Assess the morphology of the red blood cells.
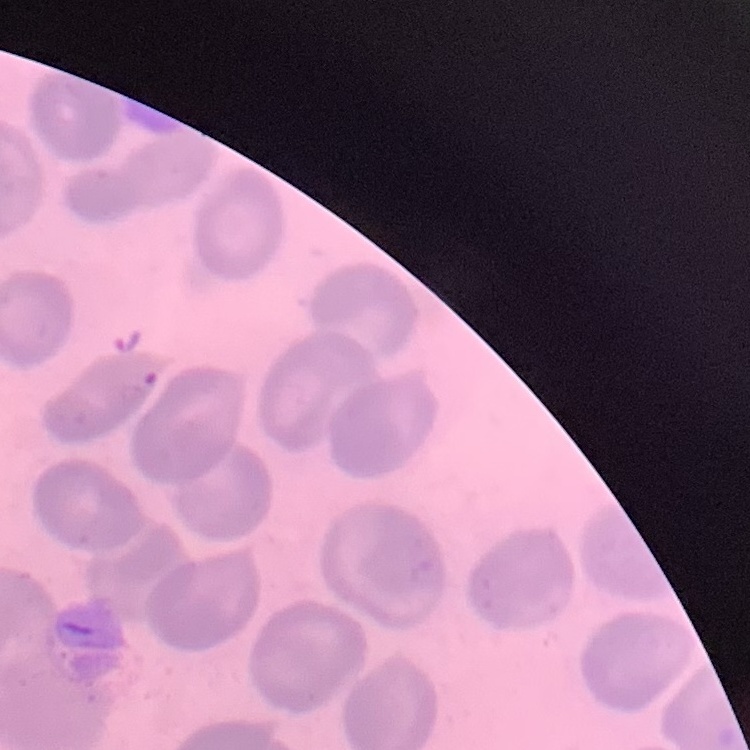

No rouleaux formation.

stain: Field's or Giemsa
preparation: thin blood smear
image_type: one tile cut from a larger photomicrograph